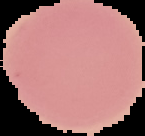
The area outside the segmented cell region is set to black. Result: no malaria parasites detected. From a thin blood smear. Image is 145×136 pixels.